Locate every uninfected red blood cell.
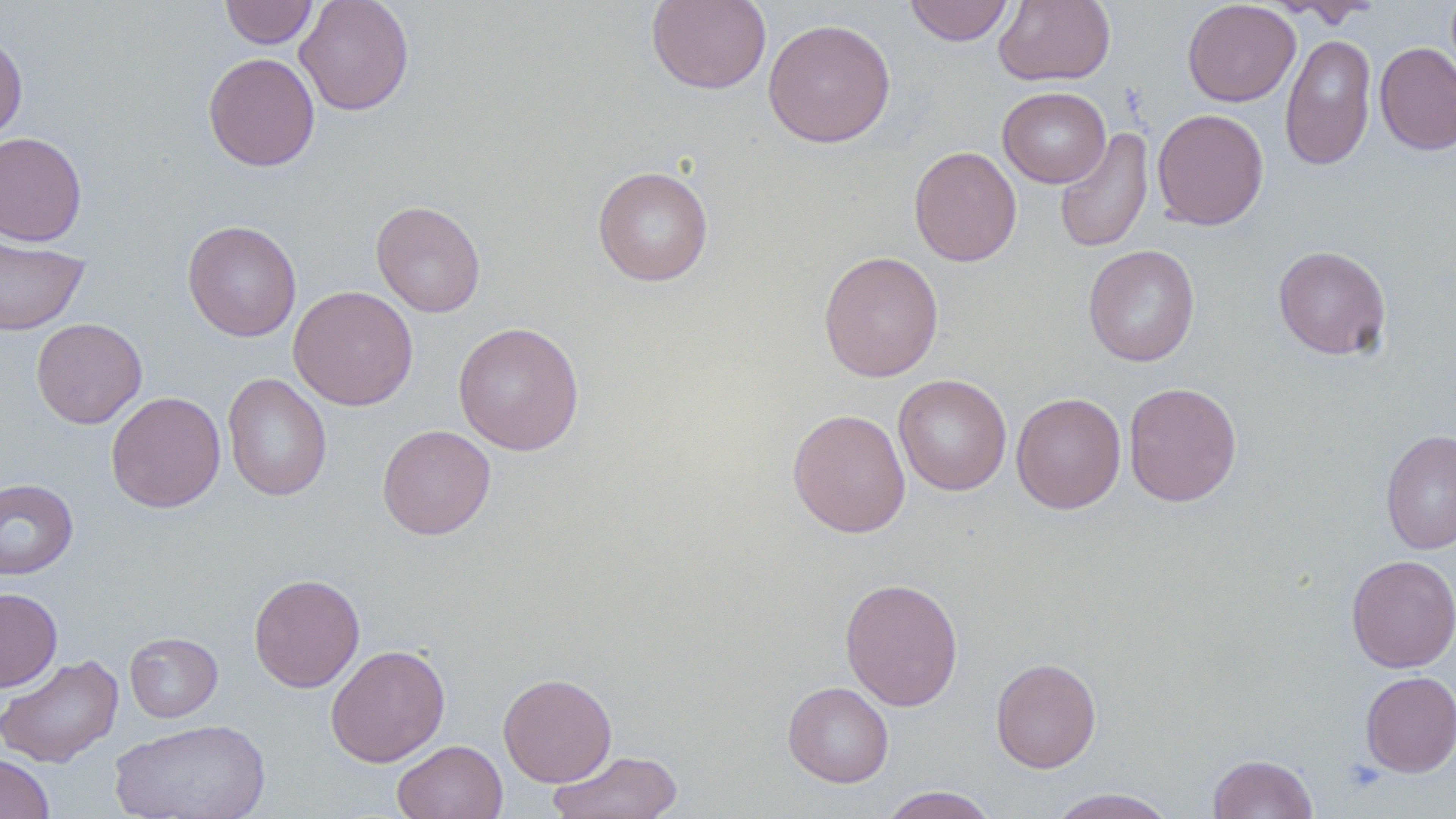

Approximate bounding boxes as (x1, y1, x2, y2) in pixels.
Uninfected red blood cells: (219, 0, 318, 49), (295, 0, 414, 115), (646, 0, 772, 94), (904, 0, 1014, 46), (993, 0, 1115, 86), (1183, 0, 1300, 107), (1270, 0, 1381, 28), (762, 18, 895, 148), (0, 32, 27, 142), (1280, 33, 1377, 171), (1374, 42, 1456, 155), (203, 52, 320, 171), (998, 86, 1111, 188), (1152, 108, 1269, 231), (1054, 127, 1154, 254), (0, 132, 87, 246), (909, 146, 1022, 267), (592, 166, 714, 286), (370, 200, 486, 317), (183, 220, 302, 342), (0, 235, 89, 336), (1083, 244, 1199, 367), (1273, 245, 1391, 360), (818, 250, 944, 382), (288, 285, 419, 411), (31, 318, 147, 429), (453, 321, 584, 455), (222, 373, 332, 501), (894, 374, 1012, 496), (1123, 382, 1242, 507), (106, 391, 226, 513), (1011, 392, 1126, 514), (787, 408, 911, 537), (378, 425, 497, 540), (1381, 429, 1456, 555), (0, 478, 78, 580), (1345, 554, 1456, 672), (248, 573, 364, 692), (840, 577, 963, 711), (0, 587, 62, 692), (124, 632, 223, 722), (325, 644, 450, 767), (0, 653, 124, 768), (990, 657, 1102, 772), (1360, 671, 1456, 777), (498, 673, 617, 787), (782, 681, 894, 787), (110, 718, 270, 819), (393, 740, 507, 819), (547, 749, 684, 819), (0, 753, 55, 819), (1208, 753, 1318, 818), (876, 786, 999, 819), (1043, 788, 1181, 818).

Slide-level diagnosis: negative for blood parasites. Image is 1456×819 pixels. Thin blood smear. One field of a larger specimen. May-Grünwald-Giemsa stain. Captured at 1000x magnification. Optical microscopy.